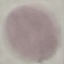

Summary:
  - Malaria status: uninfected
  - Image type: cell patch, automatically extracted from a larger field of view and resized to 64 × 64 pixels
  - Capture: smartphone through the microscope eyepiece
  - Preparation: thin smear
  - Stain: Giemsa